Report the malaria status of this cell.
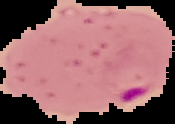

Parasitized.

Summary:
  - Preparation: thin blood smear
  - Image size: 175×124 pixels
  - Image type: segmented cell region on a black background